Identify the parasite.
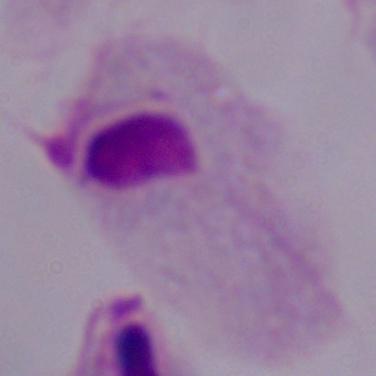
A trichomonad.

Summary:
  - Magnification: 1000x
  - Modality: micrograph